Name the parasite shown.
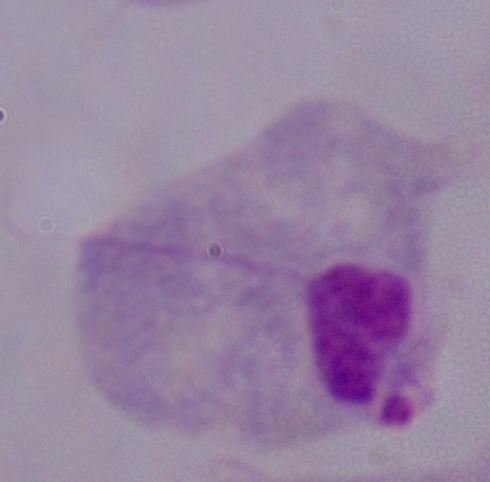

This is a trichomonad.

Micrograph. Captured at 1000x magnification.